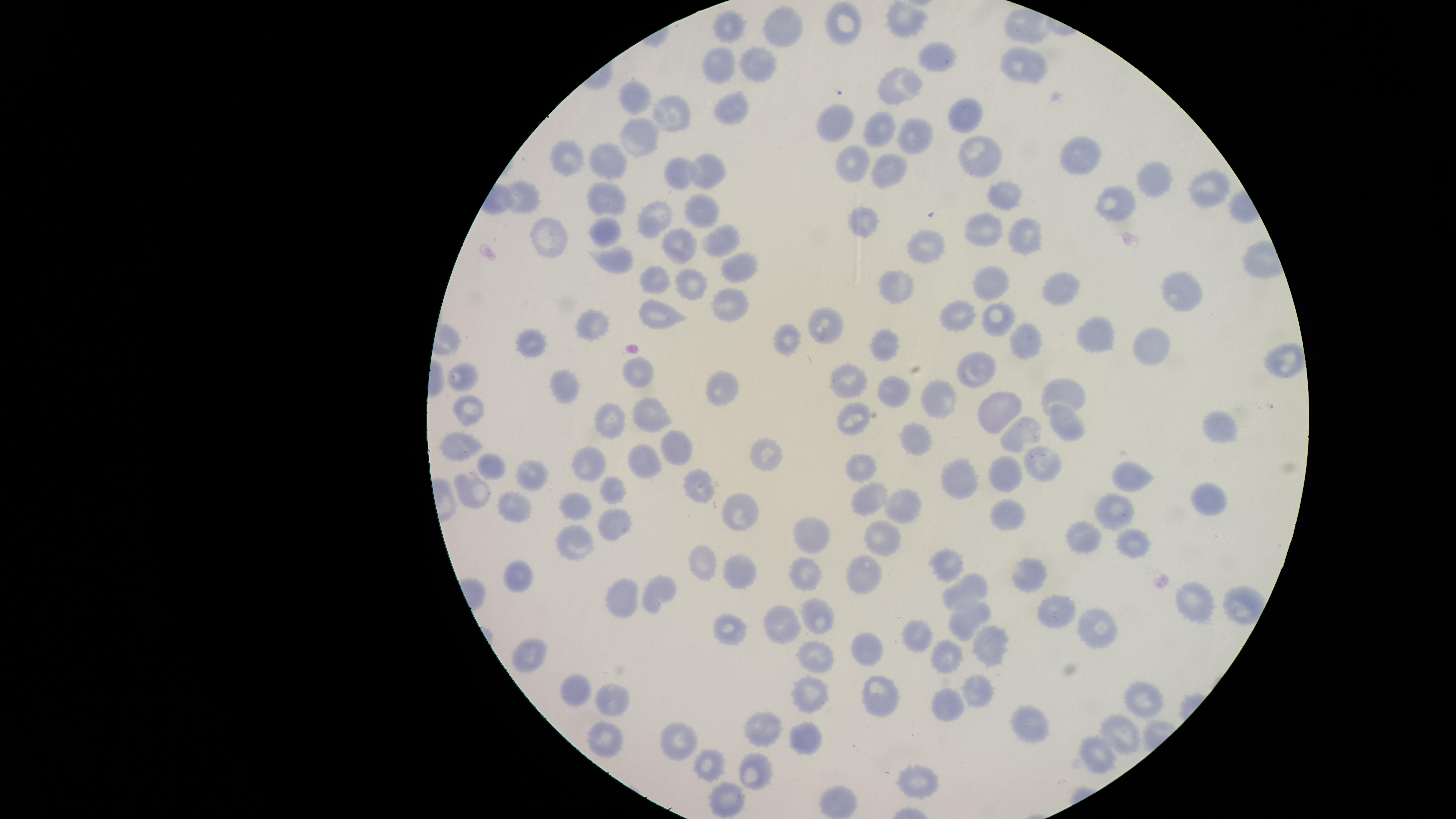 Approximate marker points as [x, y] in pixels. Uninfected red blood cells: [846, 22], [734, 24], [902, 25], [1028, 25], [783, 29], [942, 57], [719, 61], [1025, 66], [755, 68], [898, 79], [636, 96], [675, 111], [734, 111], [967, 114], [833, 121], [880, 125], [645, 138], [912, 138], [977, 150], [569, 154], [1075, 154], [608, 155], [855, 156], [676, 169], [891, 170], [708, 171], [1152, 183], [1205, 189], [1003, 194], [525, 197], [609, 199], [1112, 205], [702, 211], [647, 216], [865, 220], [981, 227], [1028, 232], [549, 234], [603, 235], [725, 240], [678, 246], [930, 249], [616, 255], [738, 267], [660, 278], [685, 280], [995, 280], [900, 287], [1063, 287], [1181, 295], [728, 304], [959, 311], [654, 314], [995, 317], [828, 319], [592, 321], [788, 333], [1098, 336], [1140, 337], [537, 339], [1022, 341], [886, 342], [1286, 362], [980, 367], [641, 375], [849, 376], [463, 377], [567, 390], [1068, 390], [888, 391], [725, 393], [934, 401], [1002, 403], [466, 404], [653, 409], [857, 418], [611, 419], [1069, 421], [1222, 428], [1025, 432], [911, 437], [461, 443], [681, 443], [764, 452], [645, 459], [589, 461], [490, 469], [862, 469], [1039, 469], [1130, 474], [532, 476], [1003, 478], [961, 484], [701, 485], [475, 488], [612, 491], [871, 499], [577, 502], [1205, 502], [899, 505], [734, 511], [1113, 511], [520, 513], [1009, 518], [609, 521], [1083, 537], [812, 538], [878, 538], [575, 543], [1134, 543], [705, 562], [946, 563], [749, 569], [1030, 570], [862, 574], [519, 578], [803, 579], [963, 587], [656, 588], [627, 596], [1195, 600], [1052, 608], [819, 614], [969, 616], [784, 619], [733, 626], [1093, 629], [917, 637], [868, 647], [990, 652], [526, 656], [953, 658], [813, 664], [987, 685], [577, 692], [808, 695], [616, 696], [877, 701], [1142, 703], [947, 705], [1024, 720], [768, 729], [597, 733], [678, 739], [1120, 739], [803, 742], [1095, 761], [708, 764], [757, 770], [913, 779], [838, 803], [724, 804]. Presence: no malaria parasites detected. Photographed with a smartphone camera through the microscope eyepiece. Circular visible region. Giemsa-stained preparation. Thin smear of blood. Image is 1456×819 pixels. One field of view of the specimen.